Comment on the morphology of the erythrocytes.
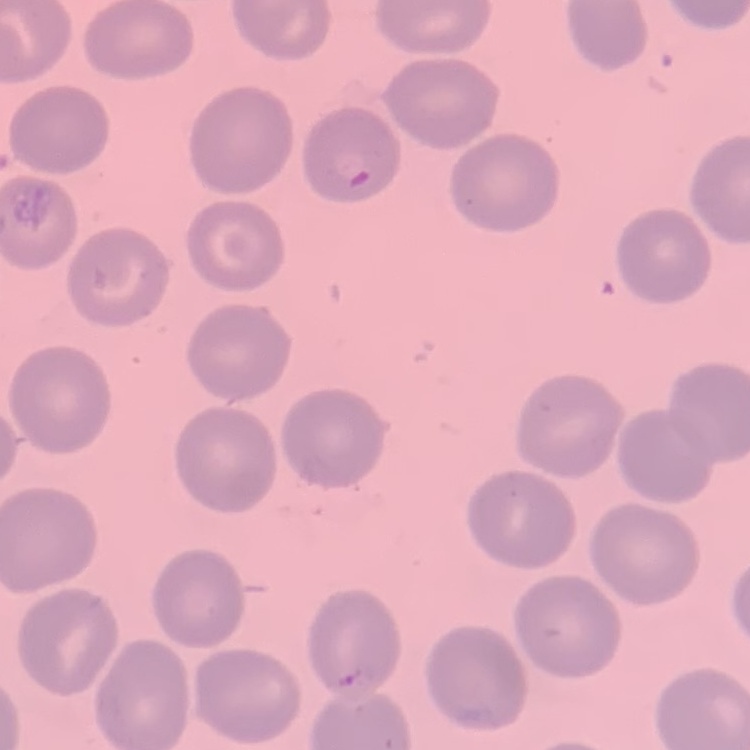

They show no rouleaux formation.

Square crop of a larger photomicrograph. Field's or Giemsa stain. Thin peripheral smear.